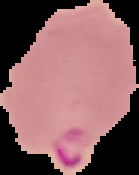

Summary:
  - Image size: 139×175 pixels
  - Preparation: thin blood smear
  - Malaria status: parasitized
  - Image type: segmented cell region on a black background